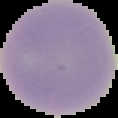

Summary:
  - Result: no Plasmodium parasites detected
  - Image type: segmented cell region on a black background
  - Preparation: thin blood film
  - Image size: 118×118 pixels